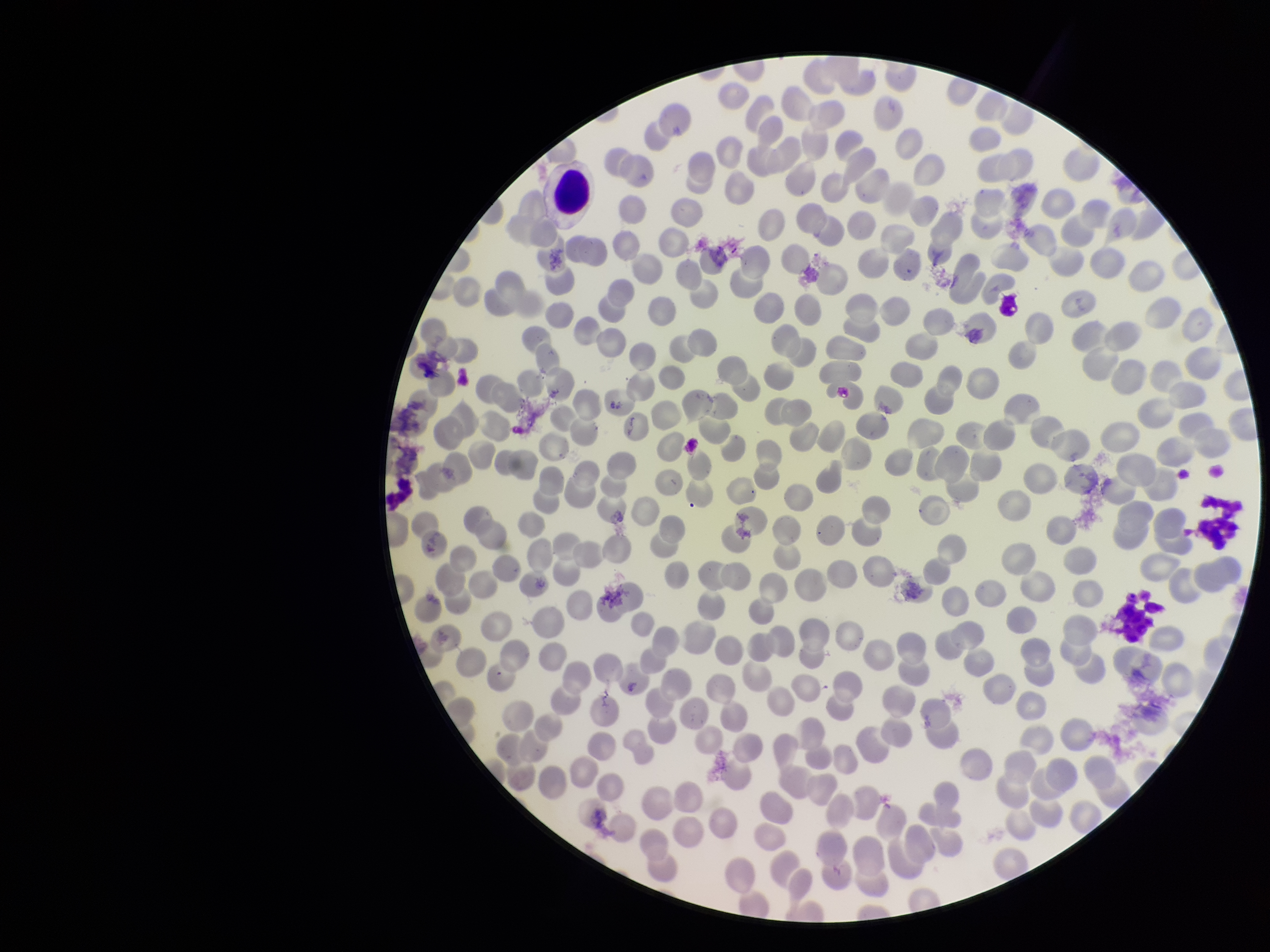
Summary:
  - Field of view: one from this slide
  - Parasitized red blood cells: none seen
  - Capture: smartphone photograph through the microscope eyepiece
  - Preparation: thin blood smear
  - Patient malaria status: negative
  - Parasitized red blood cell count: 0
  - Red blood cell count: 224
  - Stain: Giemsa
  - Image size: 1270×952 pixels